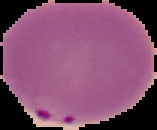
From a thin blood smear. Segmented cell region on a black background. Result: Plasmodium parasites detected. Image is 157×130 pixels.